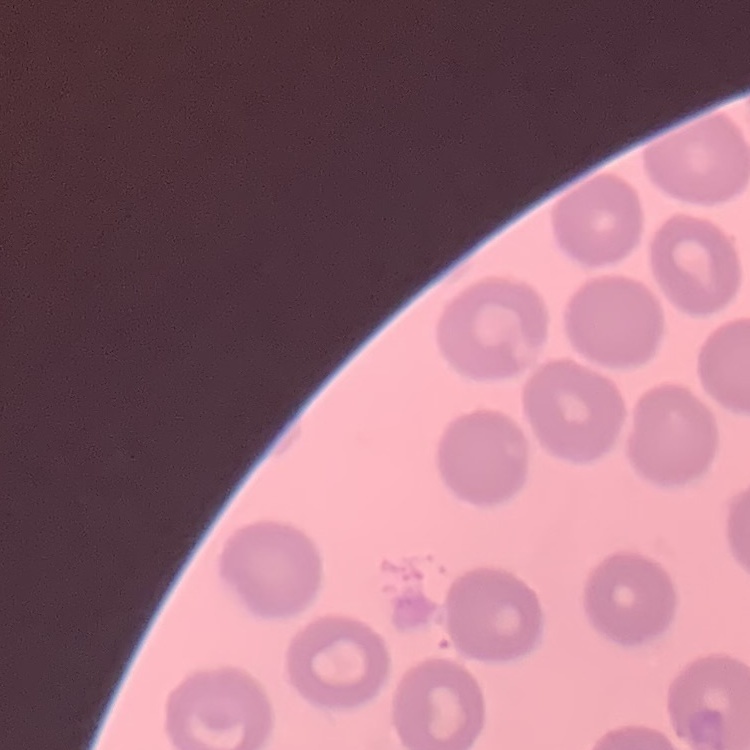

The red blood cells exhibit no rouleaux formation. Field's or Giemsa stain. One tile cut from a larger photomicrograph. Thin blood smear.